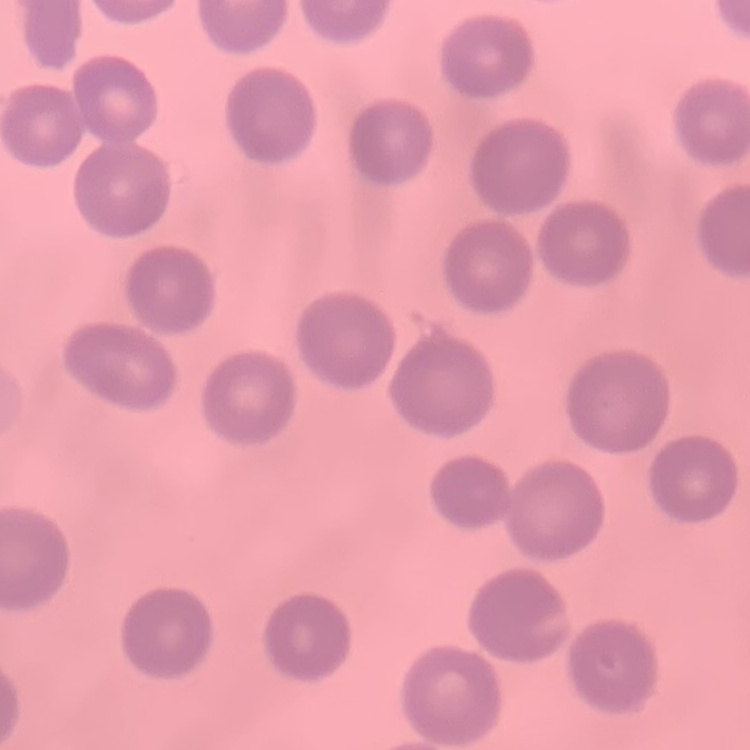
The red blood cells exhibit no rouleaux formation. Field's or Giemsa stain. One tile cut from a larger photomicrograph. Thin blood smear.